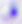

Summary:
  - Magnification: 400x
  - Identification: Toxoplasma gondii
  - Modality: photomicrograph